Locate every Plasmodium parasite.
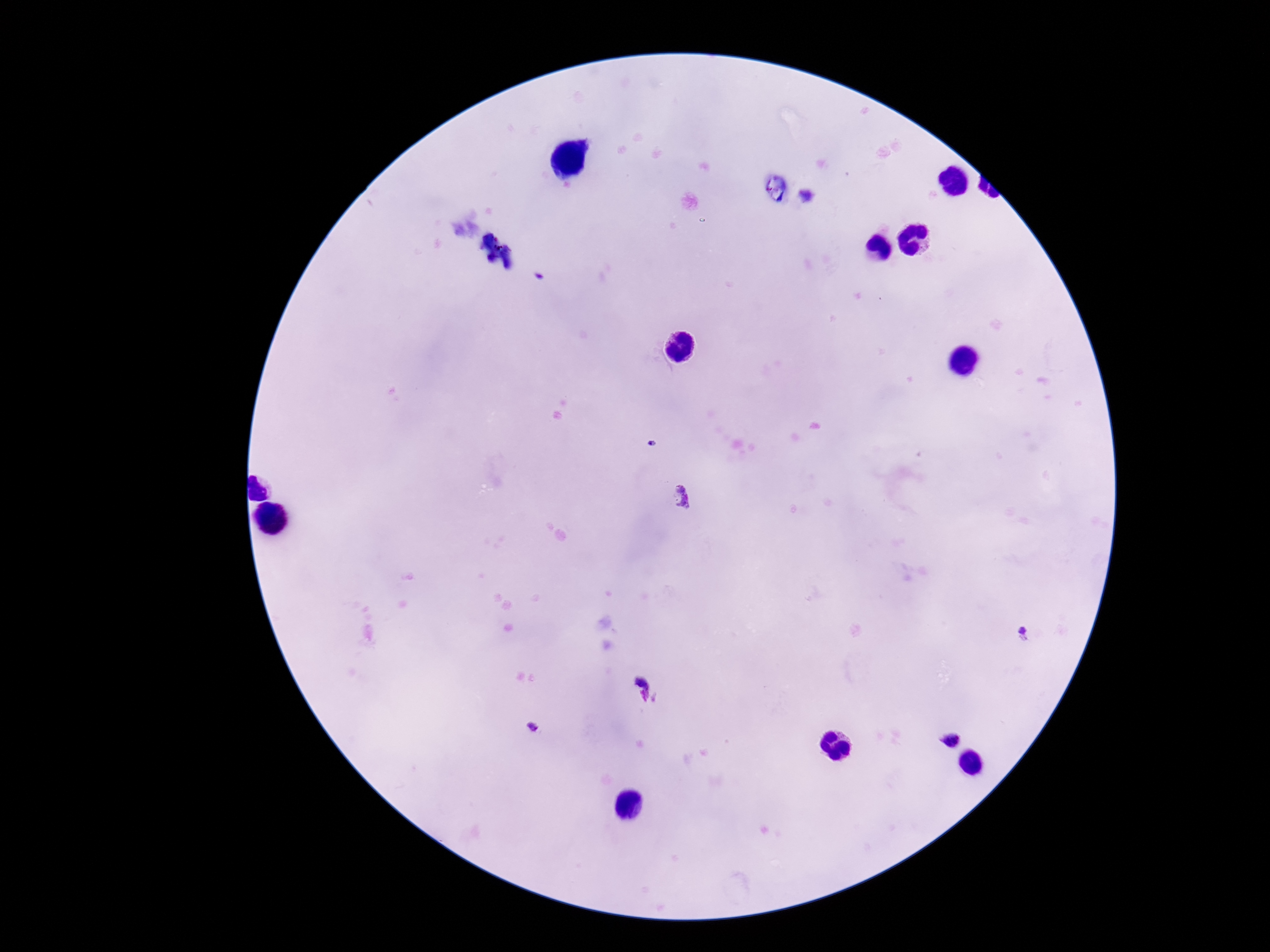

Approximate centers as [x, y] in pixels.
Plasmodium parasites: [808, 197], [652, 444], [681, 497], [1025, 634], [532, 727], [950, 740].

Photographed through the microscope eyepiece with a smartphone camera. Thick blood film. Image is 1270×952 pixels. Patient malaria status: positive. One field from this slide. 100x magnification. Giemsa-stained preparation.